Comment on the morphology of the erythrocytes.
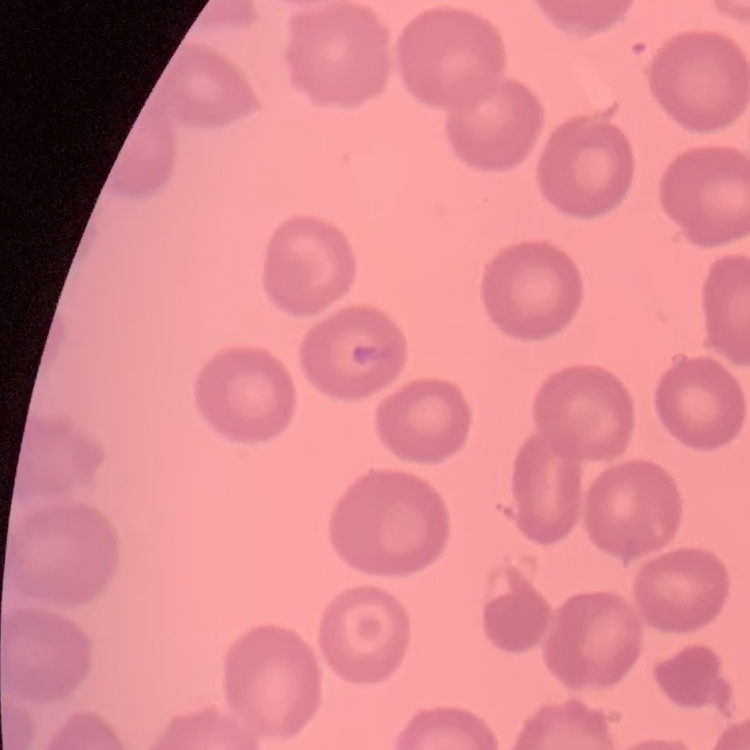
They show no rouleaux formation.

stain = Field's or Giemsa
image type = square crop of a larger photomicrograph
preparation = thin blood film